Assess this cell for malaria.
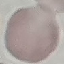
Uninfected.

stain = Giemsa
capture = smartphone through the microscope eyepiece
preparation = thin blood film
image type = automatically extracted cell patch, resized to 64 × 64 pixels